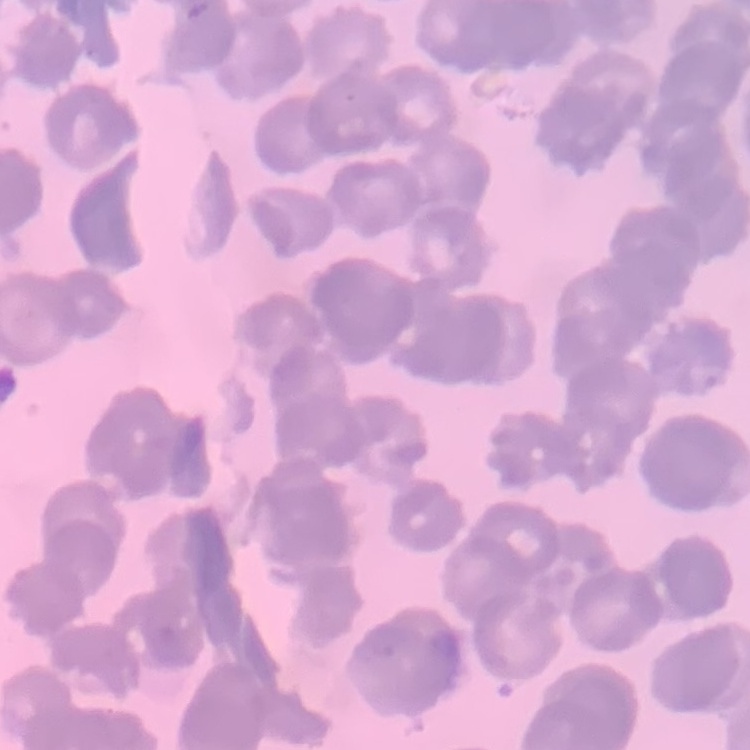

erythrocyte morphology = rouleaux formation
stain = Field's or Giemsa
image type = square crop of a larger photomicrograph
preparation = thin peripheral smear